Identify the parasite.
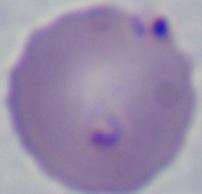

This is Babesia.

magnification = 1000x
modality = photomicrograph